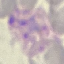

Result: malaria parasites detected. Thin blood film. Photographed with a smartphone camera at the microscope eyepiece. Giemsa stain. Cell patch, automatically extracted from a larger field of view and resized to 64 × 64 pixels.